Identify the parasite.
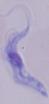

A trypanosome.

Summary:
  - Modality: photomicrograph
  - Magnification: 1000x